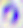
Summary:
  - Modality: photomicrograph
  - Identification: Toxoplasma gondii
  - Magnification: 400x